Describe the morphology of the erythrocytes.
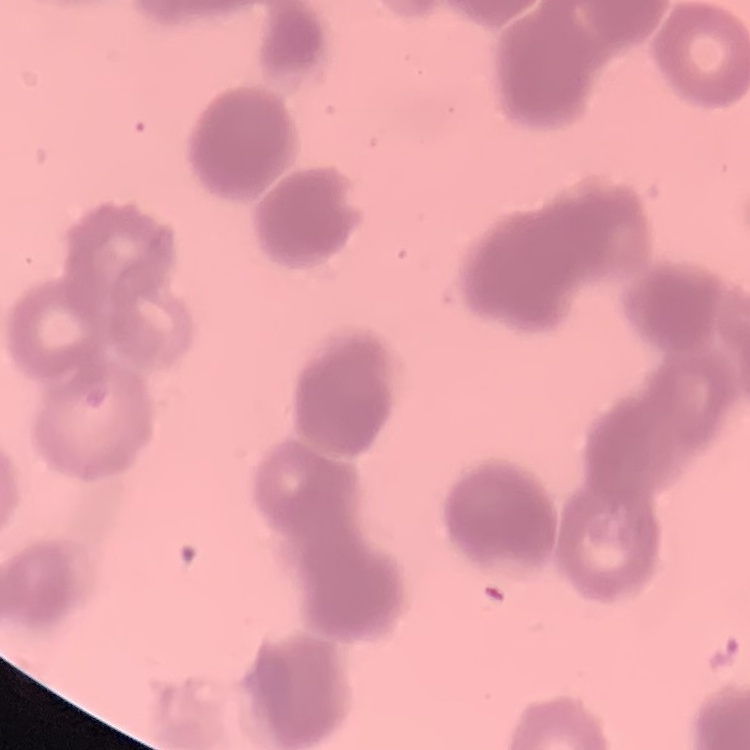
They show rouleaux formation.

image type = one tile cut from a larger photomicrograph
stain = Field's or Giemsa
preparation = thin blood smear